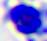
Captured at 400x magnification. A white blood cell is seen. Micrograph.